Describe the morphology of the erythrocytes.
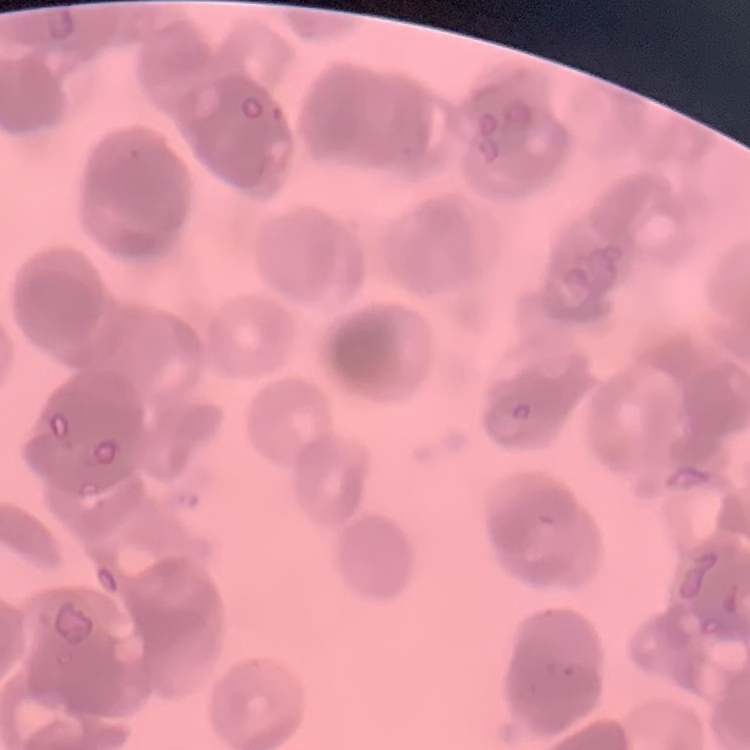
Rouleaux formation.

Field's or Giemsa stain. Thin blood film. One tile cut from a larger photomicrograph.